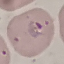

Summary:
  - Result: malaria parasites identified
  - Preparation: thin smear
  - Capture: smartphone camera at the microscope eyepiece
  - Stain: Giemsa
  - Image type: cell patch, automatically extracted from a larger field of view and resized to 64 × 64 pixels